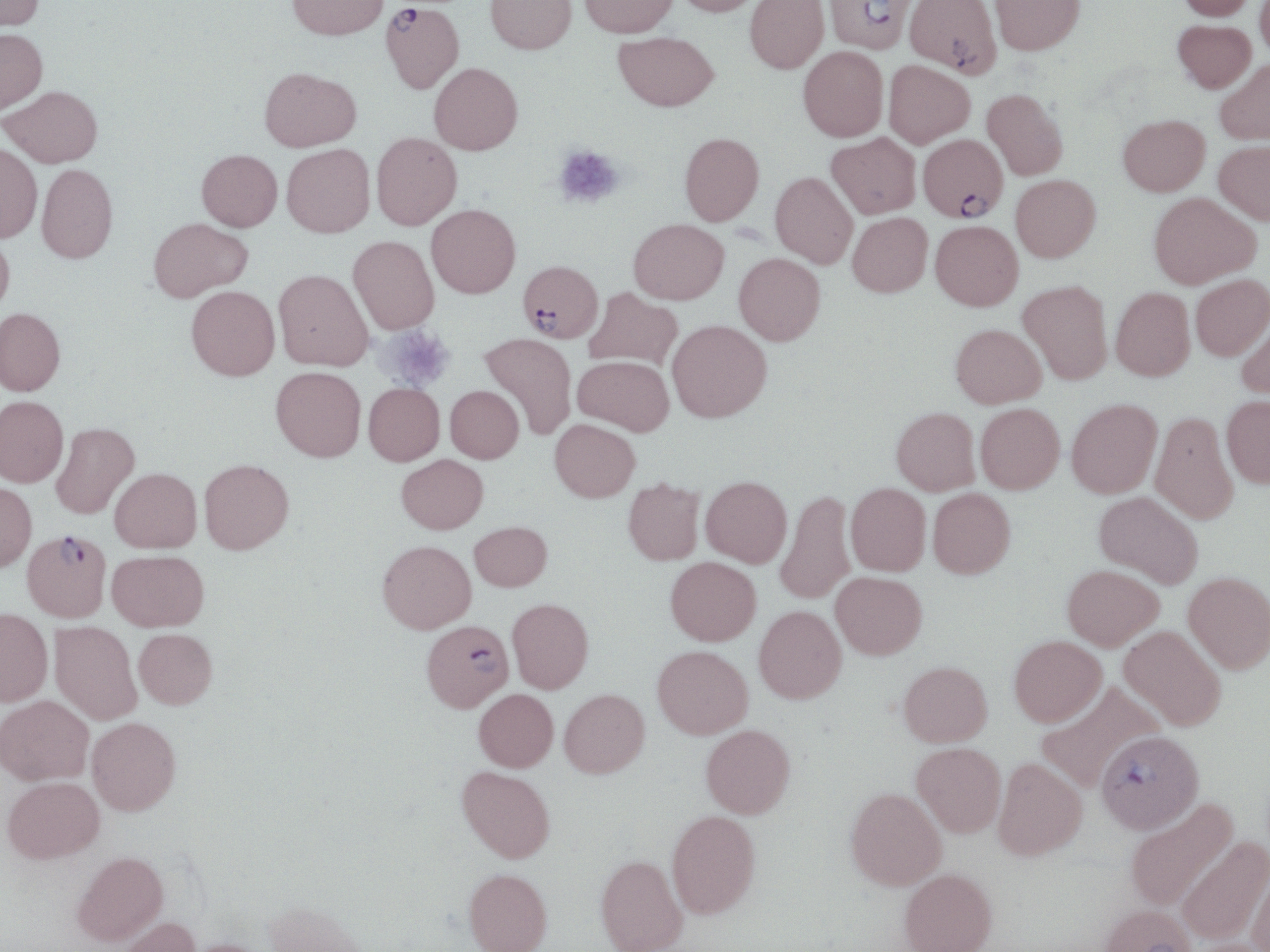

Approximate bounding boxes as (x1,y1)-(x2,y2) corner pairs in pixels. Platelet locations: (553,145)-(626,210), (376,325)-(456,392). Plasmodium falciparum-infected red blood cell locations: (823,0)-(920,63), (381,2)-(463,93), (916,134)-(1010,228), (518,260)-(603,343), (23,529)-(112,622), (421,620)-(514,711), (1096,730)-(1203,833). Uninfected red blood cell locations: (0,0)-(44,32), (287,0)-(389,40), (485,0)-(577,54), (580,0)-(678,37), (674,0)-(763,16), (745,0)-(829,73), (905,0)-(1002,78), (989,0)-(1085,55), (1177,0)-(1258,20), (1255,0)-(1270,60), (1173,19)-(1256,92), (0,28)-(47,113), (613,32)-(719,111), (798,45)-(888,142), (1215,58)-(1270,144), (883,60)-(974,148), (429,63)-(523,155), (259,66)-(361,151), (2,85)-(103,167), (982,88)-(1068,180), (1118,114)-(1210,196), (371,132)-(462,229), (679,132)-(764,225), (826,133)-(921,219), (1214,140)-(1270,224), (0,143)-(42,242), (282,144)-(375,237), (197,149)-(282,231), (36,163)-(118,263), (770,172)-(858,268), (1011,174)-(1101,262), (1149,192)-(1259,288), (426,204)-(520,298), (847,212)-(933,297), (148,217)-(252,302), (629,218)-(729,304), (931,220)-(1023,310), (0,230)-(14,317), (348,236)-(439,334), (734,253)-(825,345), (274,269)-(373,370), (1191,275)-(1270,360), (1018,280)-(1112,384), (186,286)-(280,380), (584,287)-(682,370), (1111,287)-(1195,380), (0,308)-(66,395), (1236,313)-(1270,399), (667,320)-(771,422), (951,323)-(1046,408), (479,333)-(577,439), (573,355)-(674,435), (271,366)-(366,461), (364,383)-(445,465), (445,385)-(524,462), (1221,395)-(1270,488), (0,396)-(68,487), (1066,399)-(1162,498), (975,403)-(1065,494), (891,407)-(980,495), (1150,410)-(1239,524), (550,419)-(640,502), (51,422)-(139,519), (397,454)-(488,533), (199,459)-(294,554), (110,468)-(202,553), (700,476)-(791,567), (622,478)-(704,565), (0,482)-(36,571), (846,483)-(931,575), (928,488)-(1016,578), (775,489)-(856,605), (1094,491)-(1203,588), (469,521)-(552,591), (377,540)-(476,633), (107,550)-(209,631), (665,557)-(761,645), (1062,564)-(1164,651), (831,571)-(927,659), (1183,571)-(1270,674), (507,598)-(593,693), (753,605)-(846,703), (0,608)-(53,706), (50,621)-(142,724), (1119,625)-(1226,730), (134,628)-(217,709), (1009,635)-(1107,726), (653,645)-(753,738), (898,661)-(992,746), (1037,681)-(1165,790), (559,688)-(649,778), (474,689)-(558,771), (0,695)-(94,785), (87,717)-(180,815), (701,724)-(795,818), (911,742)-(1006,837), (993,757)-(1087,860), (457,766)-(556,862), (3,776)-(104,863), (845,787)-(947,890), (1124,798)-(1239,912), (666,809)-(761,918), (1177,837)-(1270,944), (72,850)-(168,945), (595,855)-(687,952), (1248,866)-(1270,952), (463,868)-(553,952), (899,868)-(997,952), (263,900)-(367,952), (1098,904)-(1198,952), (116,915)-(201,952), (182,938)-(276,952). Slide-level diagnosis: Plasmodium falciparum. Optical microscopy. Thin blood smear. 1000x magnification. One field of a larger specimen. May-Grünwald-Giemsa-stained preparation. Image is 1270×952 pixels.